Give the position of every Plasmodium parasite.
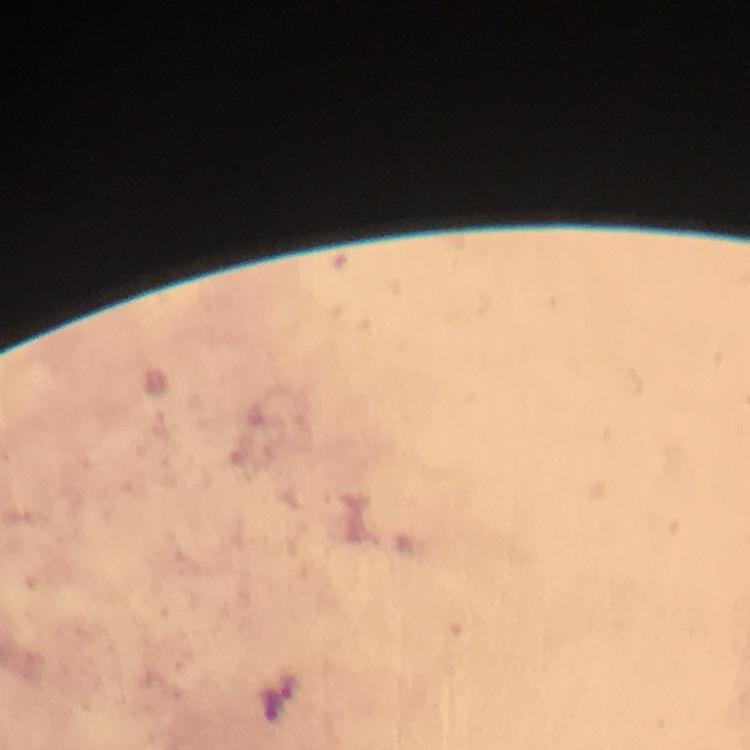
Approximate centers as (x, y) in pixels.
Plasmodium parasites: (288, 685).

Summary:
  - Stain: Giemsa
  - Context: from a diagnostic examination for malaria
  - Magnification: 100x
  - Capture: smartphone mounted on the microscope
  - Image size: 750×750 pixels
  - Preparation: thick blood film
  - Immersion oil: applied
  - Cropped from: a single field of view